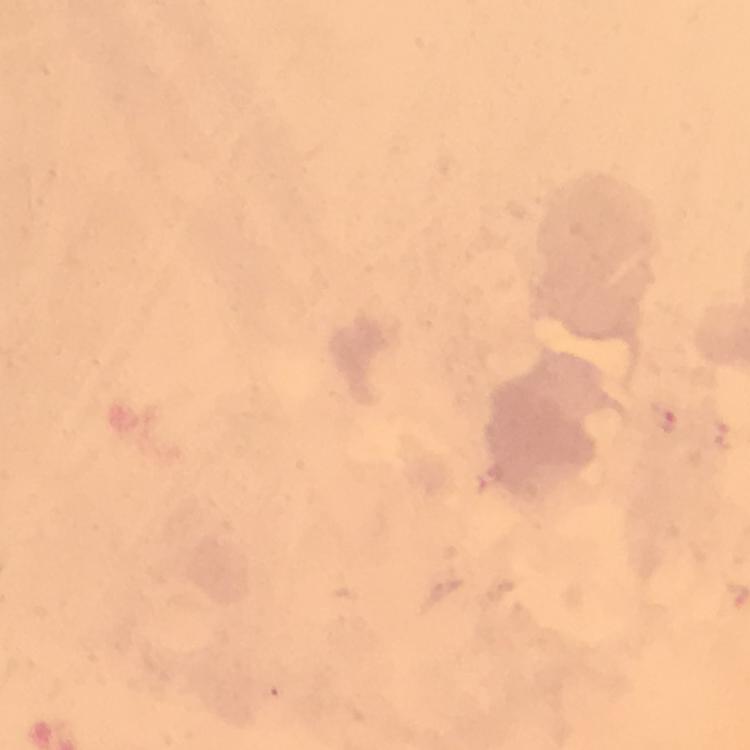
preparation: thick blood smear
capture: smartphone mounted on the microscope
image_size: 750×750 pixels
magnification: 100x
plasmodium_parasite_locations: 'approximate centers as [x, y] in pixels: [662, 419]'
cropped_from: one field of view
immersion_oil: applied
context: from a diagnostic examination for malaria
stain: Giemsa